Assess this cell for malaria.
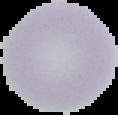

Uninfected.

Summary:
  - Preparation: thin blood film
  - Image size: 118×115 pixels
  - Image type: cell region segmented out of the field of view; surrounding area masked to black